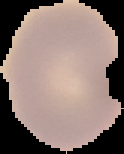
{
  "image_type": "segmented cell region on a black background",
  "result": "no Plasmodium parasites detected",
  "preparation": "thin blood film",
  "image_size": "124×154 pixels"
}